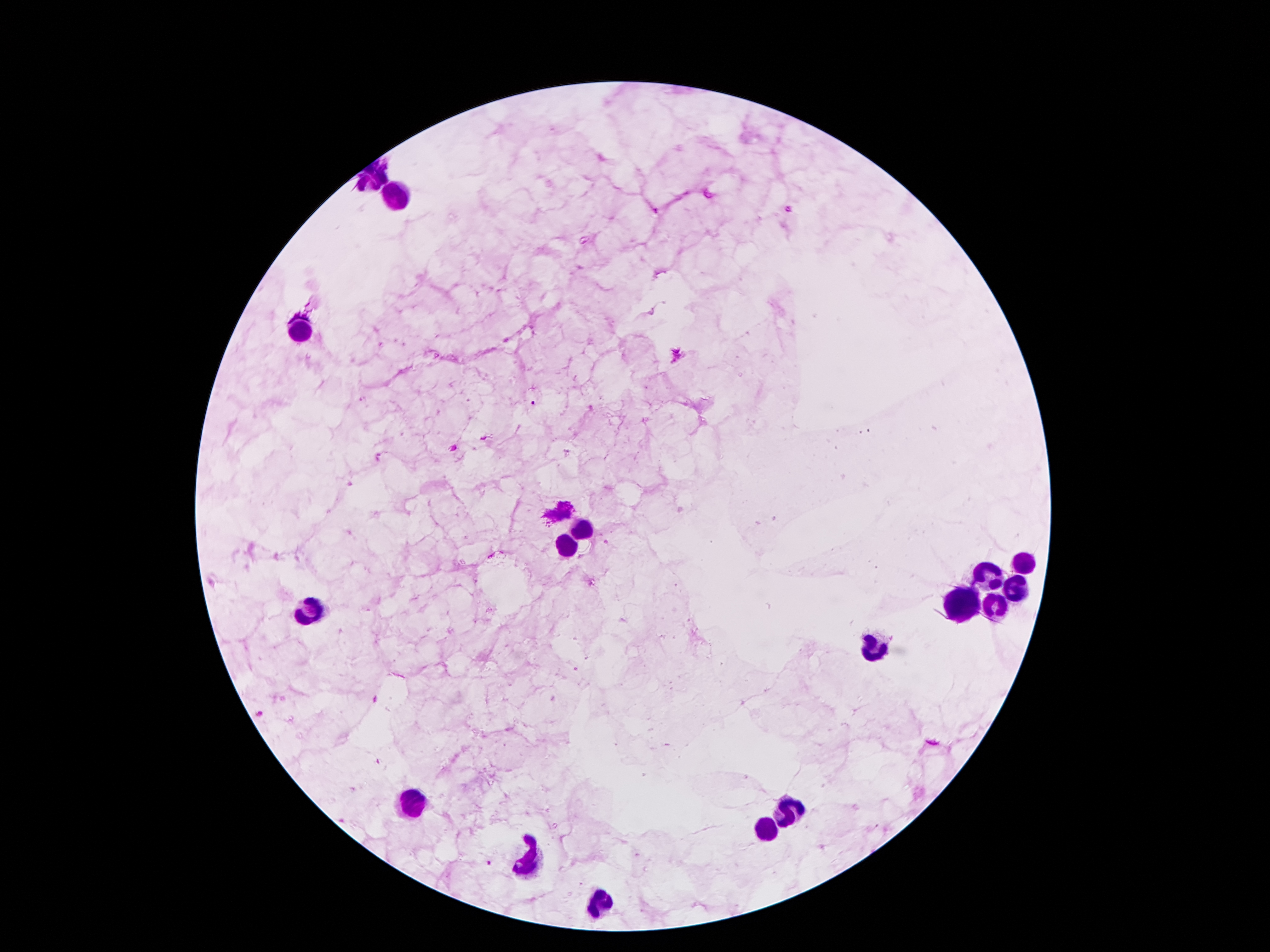 Approximate centers as (x, y) in pixels. Leukocyte locations: (380, 176), (400, 196), (294, 332), (582, 528), (568, 546), (1022, 564), (988, 576), (1014, 590), (962, 604), (996, 608), (311, 612), (872, 646), (414, 802), (792, 816), (766, 832), (530, 864), (602, 902). Malaria parasite locations: (787, 210), (678, 356), (532, 403), (487, 438), (453, 448), (489, 863). Single field of view. Thick peripheral-blood smear. Patient malaria status: positive for Plasmodium falciparum. Giemsa stain. Image is 1270×952 pixels. 100x magnification. Photographed through the microscope eyepiece with a smartphone camera.